Locate and identify every blood parasite.
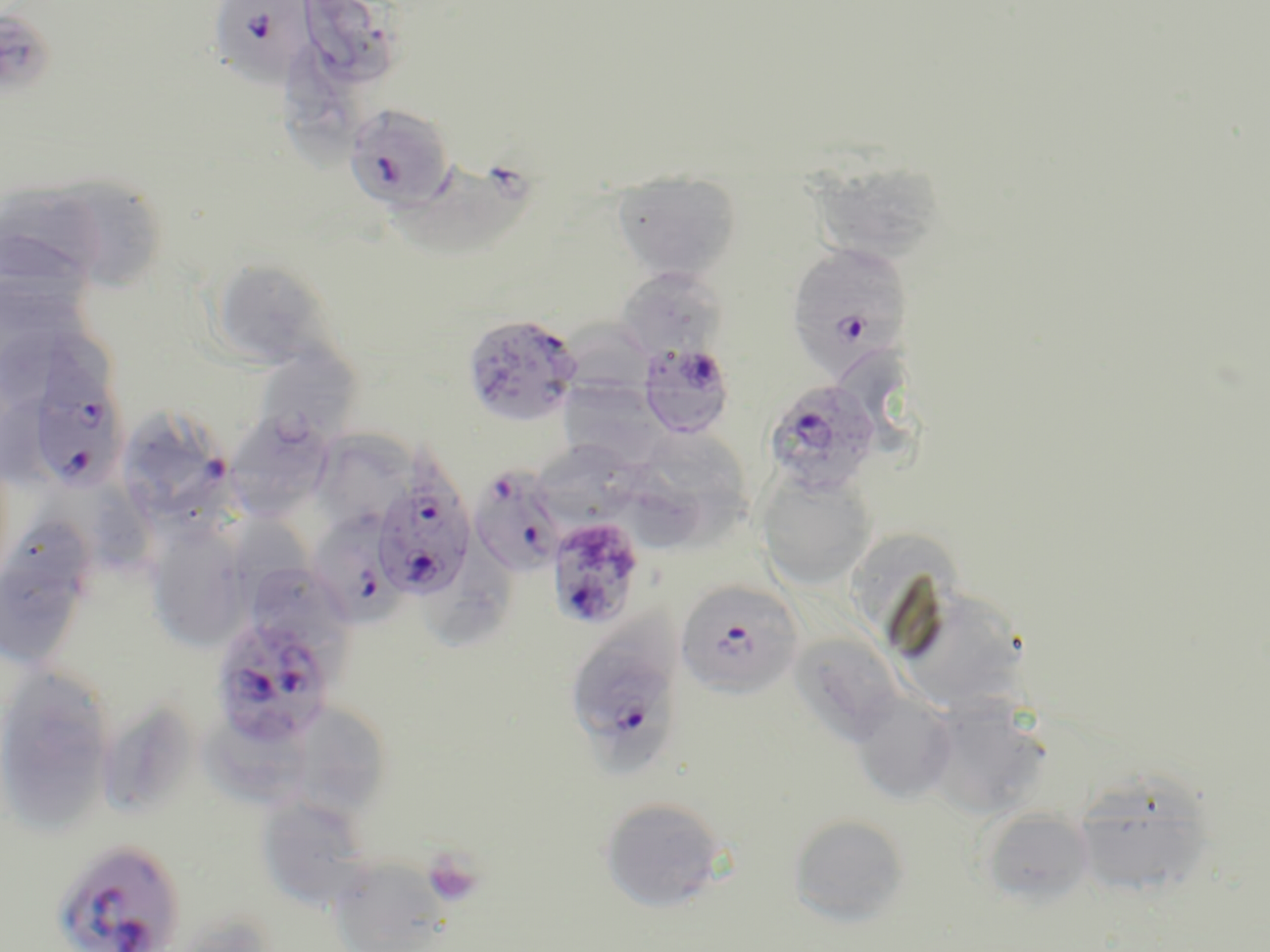

Approximate bounding boxes as named x1/y1/x2/y2 corners in pixels.
Plasmodium falciparum-infected red blood cells: (x1=208, y1=1, x2=315, y2=86), (x1=343, y1=102, x2=456, y2=211), (x1=787, y1=242, x2=913, y2=378), (x1=461, y1=313, x2=583, y2=426), (x1=637, y1=341, x2=737, y2=439), (x1=26, y1=367, x2=129, y2=494), (x1=763, y1=378, x2=883, y2=496), (x1=371, y1=461, x2=477, y2=601), (x1=469, y1=465, x2=568, y2=576), (x1=315, y1=496, x2=411, y2=626), (x1=546, y1=517, x2=645, y2=630), (x1=675, y1=580, x2=804, y2=699), (x1=571, y1=598, x2=687, y2=729), (x1=209, y1=613, x2=338, y2=747), (x1=50, y1=838, x2=186, y2=952).
No Plasmodium ovale, Plasmodium malariae, Plasmodium vivax, Babesia divergens, or Trypanosoma brucei observed.

slide_level_diagnosis: Plasmodium falciparum
platelet_locations: 'approximate bounding boxes as named x1/y1/x2/y2 corners in pixels: (x1=422, y1=849, x2=485, y2=908)'
stain: May-Grünwald-Giemsa
magnification: 1000x
modality: light microscopy
image_size: 1270×952 pixels
field_of_view: single
uninfected_red_blood_cell_locations: 'approximate bounding boxes as named x1/y1/x2/y2 corners in pixels: (x1=304, y1=0, x2=406, y2=94), (x1=0, y1=10, x2=56, y2=100), (x1=285, y1=38, x2=374, y2=167), (x1=805, y1=158, x2=948, y2=266), (x1=380, y1=161, x2=541, y2=266), (x1=611, y1=171, x2=742, y2=282), (x1=37, y1=173, x2=170, y2=293), (x1=0, y1=183, x2=115, y2=300), (x1=208, y1=259, x2=338, y2=370), (x1=615, y1=266, x2=726, y2=362), (x1=0, y1=324, x2=114, y2=411), (x1=262, y1=346, x2=359, y2=448), (x1=557, y1=378, x2=669, y2=469), (x1=228, y1=411, x2=337, y2=527), (x1=128, y1=414, x2=242, y2=539), (x1=648, y1=431, x2=749, y2=546), (x1=537, y1=442, x2=642, y2=532), (x1=613, y1=454, x2=710, y2=549), (x1=756, y1=470, x2=877, y2=590), (x1=87, y1=477, x2=157, y2=579), (x1=4, y1=513, x2=95, y2=603), (x1=230, y1=516, x2=320, y2=626), (x1=144, y1=523, x2=250, y2=651), (x1=844, y1=530, x2=964, y2=632), (x1=428, y1=534, x2=510, y2=652), (x1=0, y1=560, x2=87, y2=666), (x1=254, y1=567, x2=364, y2=673), (x1=891, y1=584, x2=1030, y2=713), (x1=789, y1=632, x2=905, y2=747), (x1=0, y1=663, x2=116, y2=829), (x1=850, y1=691, x2=959, y2=805), (x1=921, y1=697, x2=1051, y2=820), (x1=96, y1=698, x2=198, y2=820), (x1=295, y1=704, x2=392, y2=818), (x1=190, y1=715, x2=323, y2=810), (x1=1071, y1=770, x2=1218, y2=899), (x1=256, y1=796, x2=374, y2=911), (x1=599, y1=796, x2=728, y2=913), (x1=977, y1=807, x2=1095, y2=910), (x1=787, y1=813, x2=911, y2=927), (x1=326, y1=855, x2=453, y2=952), (x1=166, y1=913, x2=277, y2=952)'
preparation: thin blood smear